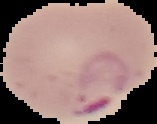

Image is 157×124 pixels. The area outside the segmented cell region is set to black. Result: malaria parasites detected. From a thin blood smear.